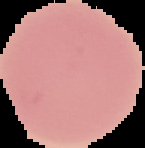

Summary:
  - Image type: segmented cell region with the area outside set to black
  - Image size: 145×148 pixels
  - Preparation: thin blood smear
  - Result: no Plasmodium parasites seen